Identify the cell.
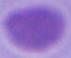
This is an erythrocyte.

Summary:
  - Magnification: 1000x
  - Modality: micrograph